Classify this cell by malaria status.
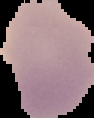
It is uninfected.

Summary:
  - Image type: cell region segmented out of the field of view; surrounding area masked to black
  - Image size: 94×118 pixels
  - Preparation: thin blood smear